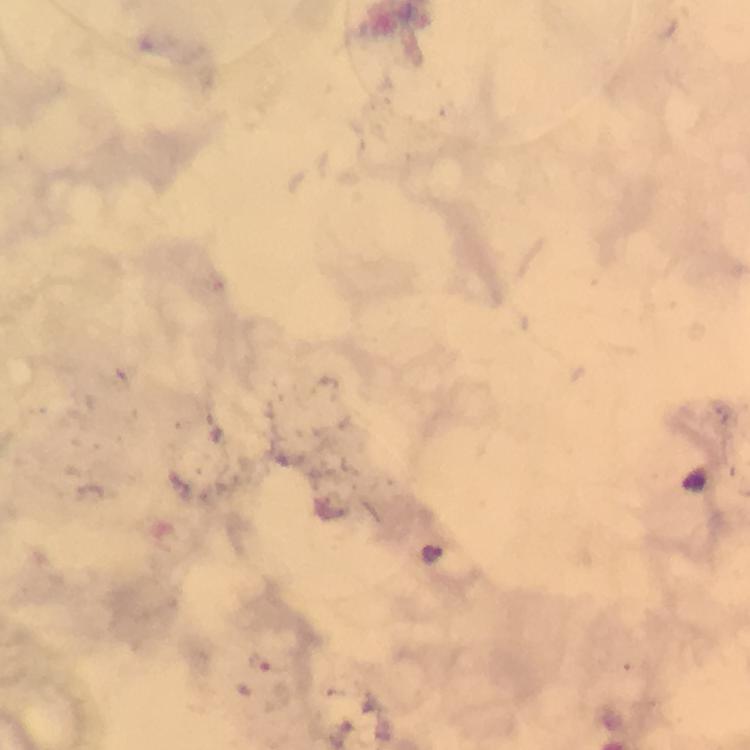

Approximate centers as {x, y} in pixels.
Summary:
  - Plasmodium parasite locations: {440, 556}, {257, 662}
  - Magnification: 100x
  - Capture: smartphone camera through the microscope
  - Preparation: thick smear
  - Immersion oil: used
  - Cropped from: one field of view
  - Context: from a diagnostic examination for malaria
  - Stain: Giemsa
  - Image size: 750×750 pixels